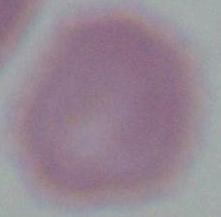

Micrograph. 1000x magnification. A red blood cell is shown.